Give the extent of all Plasmodium falciparum-infected red blood cells.
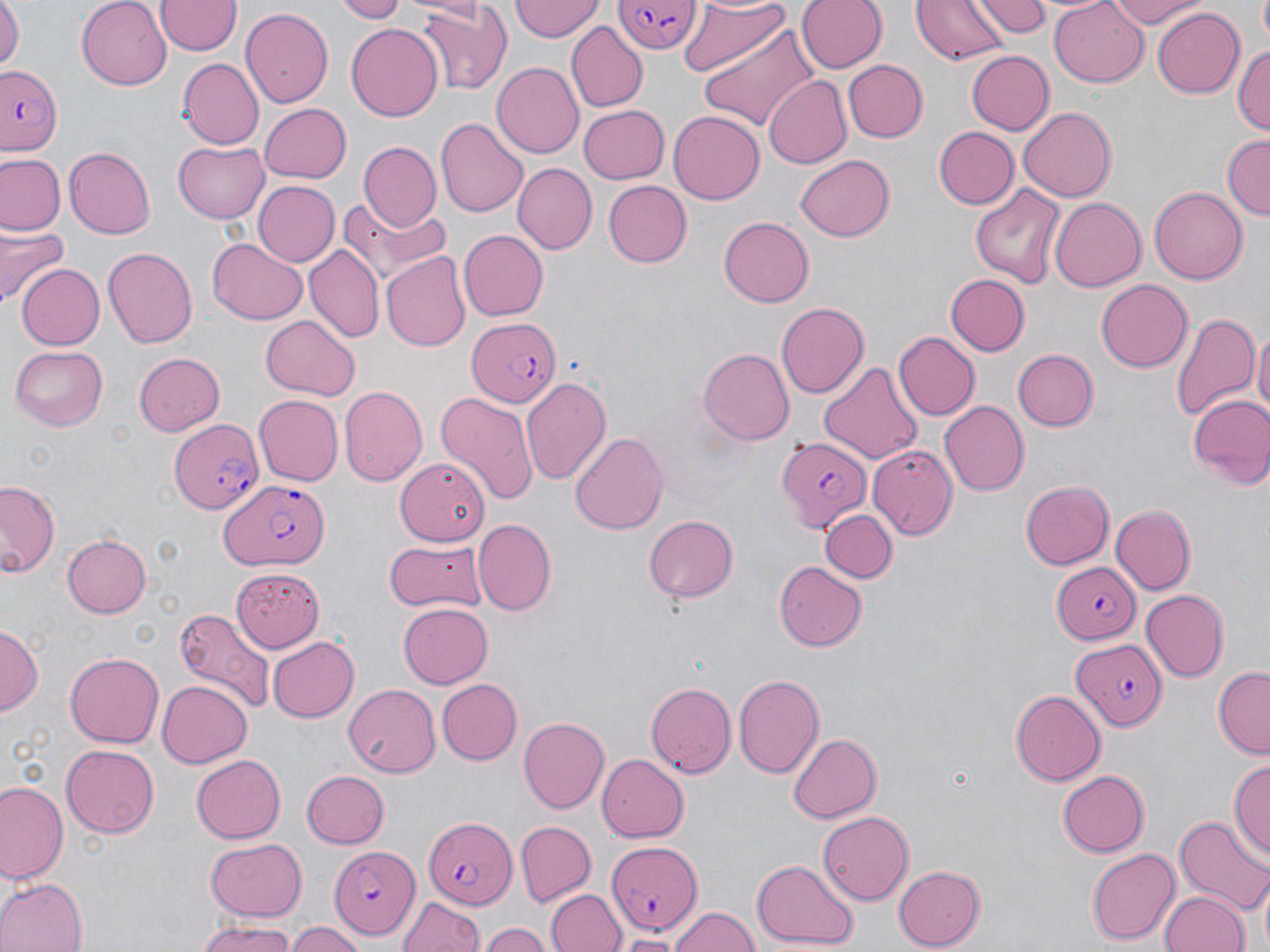

Approximate bounding boxes as [x1, y1, x2, y2] in pixels.
Plasmodium falciparum-infected red blood cells: [613, 0, 702, 53], [0, 61, 64, 153], [466, 317, 562, 409], [167, 414, 261, 517], [775, 436, 871, 534], [219, 481, 330, 568], [1052, 561, 1141, 645], [1071, 637, 1165, 729], [421, 818, 515, 909], [608, 842, 705, 934], [328, 846, 418, 938].

Uninfected red blood cell locations: [76, 0, 171, 88], [332, 0, 412, 22], [512, 0, 603, 42], [794, 0, 885, 75], [912, 0, 1009, 65], [975, 0, 1049, 37], [1049, 0, 1150, 87], [1102, 0, 1211, 29], [0, 1, 24, 77], [155, 1, 240, 57], [680, 1, 791, 81], [416, 2, 516, 97], [1152, 6, 1245, 97], [240, 8, 333, 107], [345, 21, 443, 122], [567, 24, 646, 111], [700, 24, 819, 131], [1233, 42, 1270, 139], [964, 48, 1053, 134], [182, 58, 265, 149], [842, 59, 927, 143], [492, 63, 583, 157], [764, 76, 854, 169], [260, 103, 352, 182], [579, 104, 669, 184], [1020, 107, 1116, 204], [669, 111, 765, 204], [436, 116, 529, 220], [932, 126, 1019, 209], [1221, 134, 1270, 221], [173, 139, 271, 222], [359, 142, 441, 231], [64, 148, 155, 238], [0, 155, 64, 235], [797, 156, 895, 241], [512, 164, 596, 253], [603, 180, 692, 267], [251, 181, 338, 267], [968, 182, 1067, 290], [1149, 185, 1246, 285], [1050, 196, 1144, 293], [342, 198, 452, 287], [719, 215, 814, 307], [0, 223, 67, 305], [458, 231, 548, 321], [208, 238, 307, 324], [304, 245, 384, 345], [102, 246, 198, 350], [382, 254, 469, 349], [15, 265, 105, 350], [945, 274, 1029, 355], [1096, 278, 1192, 373], [774, 301, 867, 397], [1169, 306, 1257, 424], [261, 315, 359, 398], [1252, 327, 1270, 426], [893, 330, 979, 421], [10, 346, 109, 430], [1010, 348, 1099, 431], [698, 349, 793, 443], [134, 352, 226, 436], [819, 365, 924, 464], [520, 375, 610, 484], [339, 386, 426, 486], [434, 393, 538, 506], [1186, 394, 1270, 485], [252, 395, 342, 485], [940, 401, 1028, 496], [570, 431, 670, 535], [868, 445, 957, 540], [396, 456, 488, 543], [1, 479, 63, 582], [1020, 480, 1115, 570], [1109, 504, 1195, 596], [823, 511, 893, 583], [643, 515, 739, 602], [473, 519, 556, 616], [62, 533, 150, 616], [385, 538, 485, 612], [773, 559, 868, 651], [232, 567, 324, 650], [1139, 589, 1227, 682], [397, 603, 493, 689], [173, 607, 276, 715], [0, 626, 41, 713], [265, 636, 359, 724], [65, 652, 164, 747], [1211, 667, 1270, 757], [733, 672, 825, 777], [437, 678, 521, 764], [154, 679, 251, 768], [645, 681, 735, 778], [344, 684, 439, 777], [1010, 689, 1105, 785], [518, 715, 609, 812], [786, 732, 881, 823], [61, 744, 161, 838], [192, 753, 287, 842], [597, 753, 690, 841], [1229, 757, 1269, 862], [1058, 769, 1149, 858], [299, 770, 389, 849], [1, 781, 66, 885], [818, 811, 914, 904], [1173, 813, 1270, 915], [515, 821, 594, 906], [204, 839, 308, 919], [1088, 847, 1180, 945], [753, 856, 856, 947], [893, 865, 988, 948], [0, 877, 85, 952], [547, 889, 625, 952], [1160, 890, 1248, 952], [396, 893, 484, 952], [669, 906, 760, 952], [194, 921, 297, 951], [285, 924, 366, 952], [478, 924, 554, 952], [614, 934, 682, 952]. Slide-level diagnosis: Plasmodium falciparum. Image is 1270×952 pixels. Thin blood smear. Optical microscopy. 1000x magnification. May-Grünwald-Giemsa-stained preparation. One field of a larger specimen.